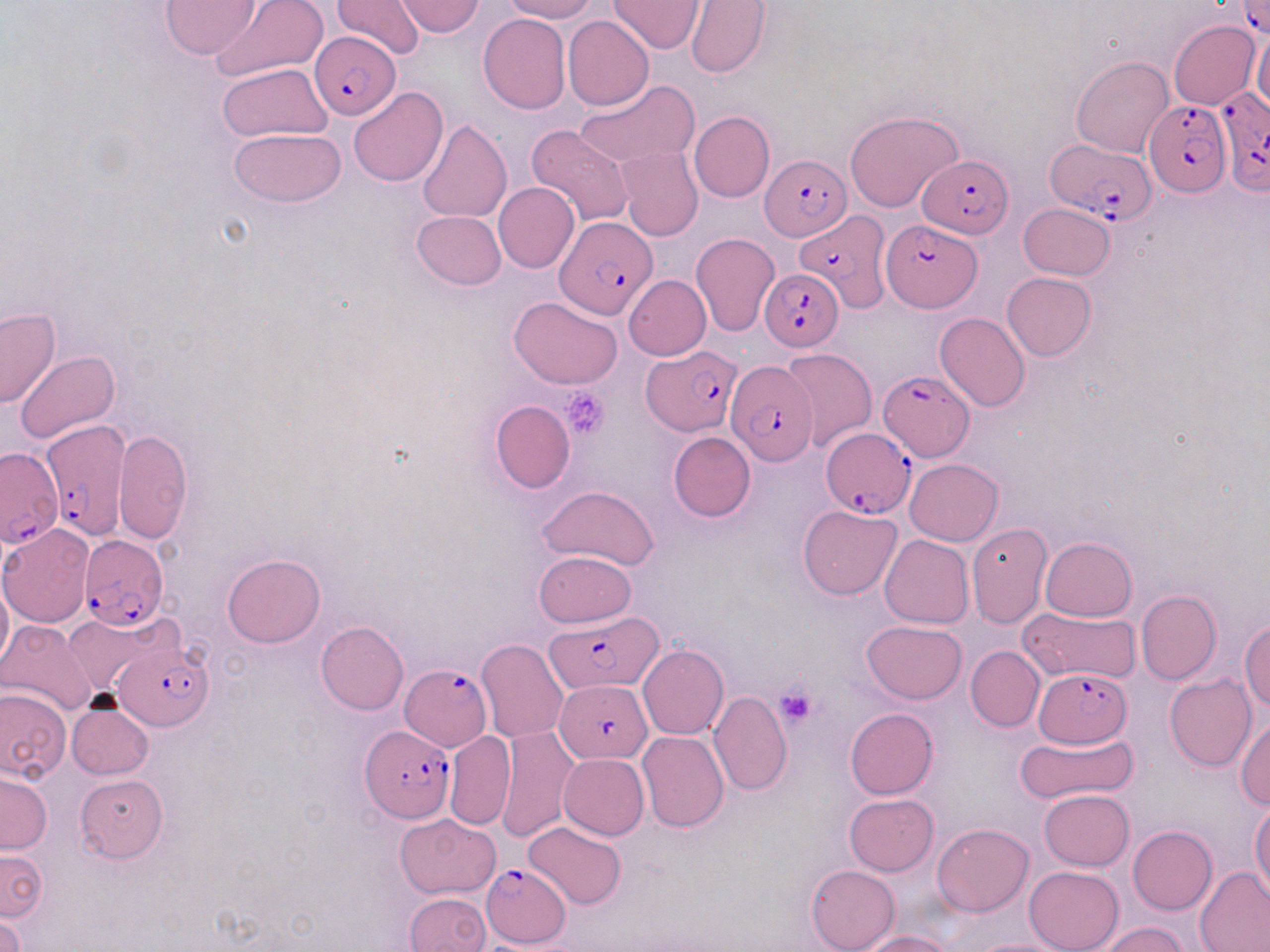

slide-level diagnosis = Plasmodium falciparum
stain = May-Grünwald-Giemsa
preparation = thin blood smear
modality = light microscopy
Plasmodium falciparum-infected red blood cell locations = approximate bounding boxes as (x1, y1, x2, y2) in pixels: (1235, 1, 1270, 35), (309, 32, 400, 118), (1216, 87, 1269, 192), (1144, 100, 1229, 197), (1045, 139, 1156, 225), (760, 155, 852, 242), (918, 156, 1013, 239), (792, 206, 891, 314), (555, 215, 657, 321), (880, 219, 980, 312), (759, 267, 841, 350), (643, 348, 737, 435), (726, 359, 818, 464), (878, 371, 973, 462), (41, 421, 130, 549), (822, 426, 917, 519), (1, 445, 64, 550), (73, 534, 168, 630), (545, 612, 664, 693), (114, 639, 215, 734), (399, 663, 492, 750), (1035, 669, 1136, 747), (555, 679, 652, 762), (360, 724, 455, 823), (482, 863, 572, 947)
platelet locations = approximate bounding boxes as (x1, y1, x2, y2) in pixels: (562, 385, 610, 441), (773, 685, 819, 730)
image size = 1270×952 pixels
magnification = 1000x
field of view = one of a larger specimen
uninfected red blood cell locations = approximate bounding boxes as (x1, y1, x2, y2) in pixels: (160, 0, 258, 58), (212, 0, 327, 85), (334, 0, 425, 60), (498, 0, 599, 22), (686, 0, 770, 79), (395, 1, 486, 36), (610, 1, 704, 54), (478, 13, 571, 114), (562, 16, 653, 111), (1169, 20, 1260, 110), (1253, 33, 1269, 113), (1071, 56, 1173, 158), (218, 62, 332, 142), (575, 79, 699, 170), (348, 87, 449, 187), (845, 109, 964, 211), (689, 111, 775, 201), (418, 118, 512, 224), (526, 125, 634, 230), (230, 128, 346, 208), (616, 146, 704, 242), (494, 181, 579, 274), (1018, 204, 1116, 280), (411, 211, 507, 290), (692, 233, 779, 336), (1001, 273, 1096, 361), (624, 275, 711, 359), (509, 296, 622, 390), (1, 307, 61, 409), (934, 312, 1029, 411), (780, 348, 877, 451), (16, 350, 119, 443), (490, 400, 574, 493), (113, 429, 193, 544), (668, 431, 756, 521), (905, 459, 1003, 545), (538, 485, 660, 572), (798, 504, 902, 599), (0, 523, 95, 628), (963, 526, 1047, 627), (879, 534, 973, 629), (1040, 536, 1136, 622), (533, 551, 637, 628), (223, 554, 325, 647), (0, 570, 12, 676), (1136, 590, 1221, 687), (1017, 606, 1142, 684), (61, 611, 176, 698), (0, 620, 100, 719), (316, 620, 409, 715), (862, 620, 967, 703), (1240, 621, 1270, 711), (475, 638, 569, 743), (637, 646, 729, 740), (965, 646, 1044, 732), (1164, 674, 1256, 772), (0, 687, 72, 782), (709, 691, 792, 796), (66, 700, 154, 780), (845, 708, 938, 799), (1234, 715, 1270, 811), (495, 725, 577, 842), (638, 730, 728, 832), (1013, 731, 1138, 806), (444, 732, 516, 830), (559, 753, 649, 840), (0, 771, 53, 853), (74, 774, 169, 862), (1039, 789, 1134, 871), (844, 793, 938, 876), (1250, 800, 1270, 900), (396, 814, 500, 898), (524, 820, 627, 910), (931, 823, 1033, 916), (1128, 825, 1217, 914), (0, 848, 46, 922), (806, 865, 900, 952), (1024, 866, 1124, 952), (1195, 866, 1270, 951), (404, 892, 490, 952), (0, 912, 25, 952), (1095, 922, 1190, 952), (854, 930, 953, 952), (964, 937, 1077, 952)